Locate every blood parasite and identify its species.
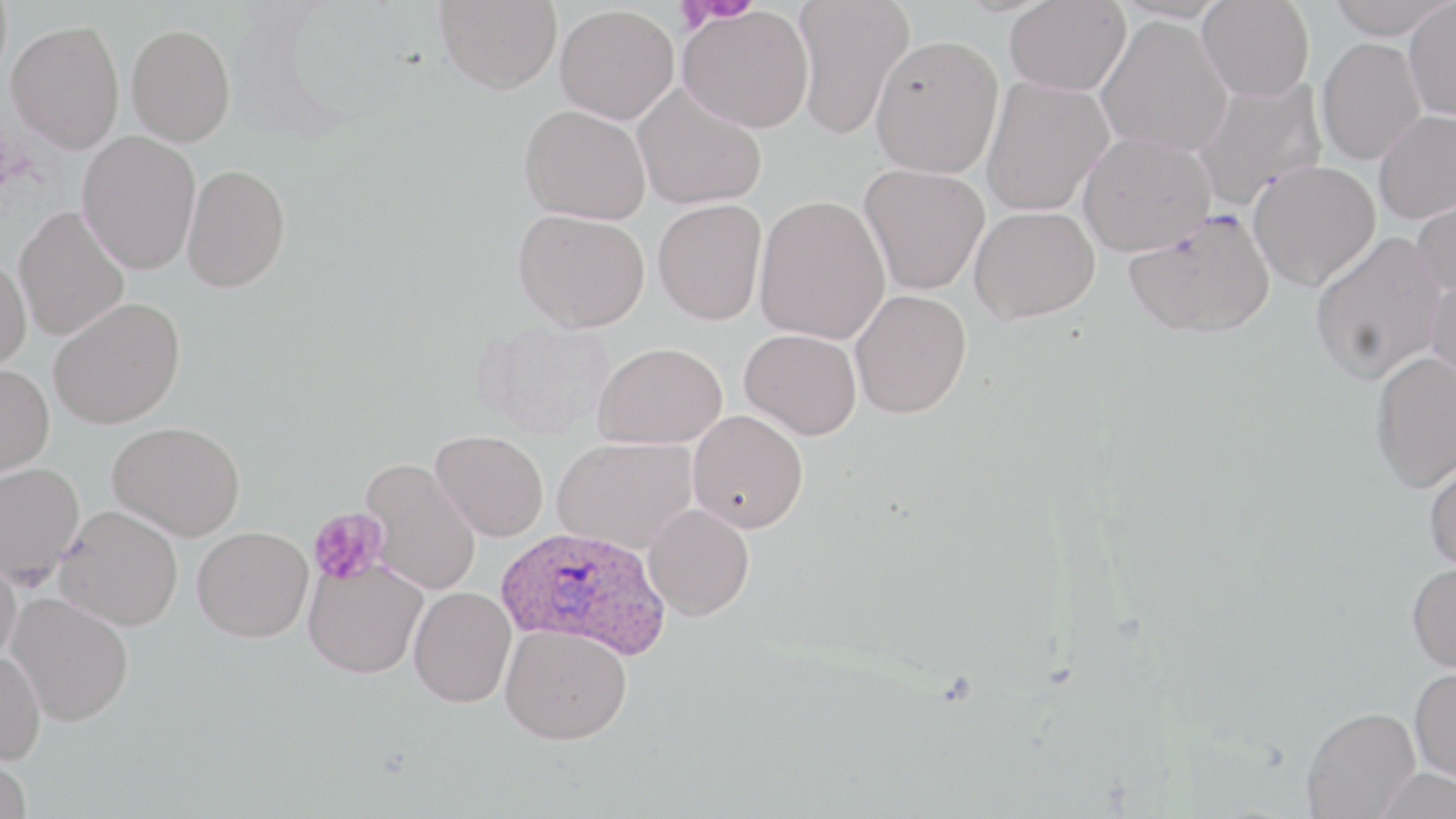

Approximate bounding boxes as named x1/y1/x2/y2 corners in pixels.
Plasmodium ovale-infected red blood cells: (x1=496, y1=526, x2=670, y2=660).
No Plasmodium falciparum, Plasmodium malariae, Plasmodium vivax, Babesia divergens, or Trypanosoma brucei observed.

slide-level diagnosis = Plasmodium ovale
field of view = one of a larger specimen
magnification = 1000x
image size = 1456×819 pixels
platelet locations = approximate bounding boxes as named x1/y1/x2/y2 corners in pixels: (x1=673, y1=0, x2=749, y2=33), (x1=308, y1=508, x2=389, y2=586)
uninfected red blood cell locations = approximate bounding boxes as named x1/y1/x2/y2 corners in pixels: (x1=435, y1=0, x2=562, y2=93), (x1=791, y1=0, x2=916, y2=140), (x1=1005, y1=0, x2=1131, y2=97), (x1=1197, y1=0, x2=1314, y2=102), (x1=1324, y1=0, x2=1455, y2=39), (x1=1403, y1=1, x2=1456, y2=120), (x1=554, y1=5, x2=678, y2=124), (x1=678, y1=6, x2=814, y2=133), (x1=1096, y1=15, x2=1233, y2=157), (x1=6, y1=20, x2=125, y2=152), (x1=126, y1=23, x2=236, y2=146), (x1=870, y1=34, x2=1003, y2=178), (x1=1316, y1=37, x2=1426, y2=165), (x1=981, y1=76, x2=1114, y2=216), (x1=1191, y1=77, x2=1327, y2=211), (x1=632, y1=82, x2=767, y2=210), (x1=519, y1=104, x2=652, y2=224), (x1=1374, y1=108, x2=1456, y2=223), (x1=77, y1=131, x2=201, y2=275), (x1=1078, y1=132, x2=1215, y2=256), (x1=1248, y1=160, x2=1381, y2=291), (x1=182, y1=163, x2=290, y2=292), (x1=859, y1=163, x2=989, y2=295), (x1=1411, y1=189, x2=1456, y2=298), (x1=755, y1=195, x2=890, y2=344), (x1=653, y1=200, x2=767, y2=325), (x1=14, y1=205, x2=129, y2=341), (x1=970, y1=206, x2=1100, y2=323), (x1=512, y1=208, x2=650, y2=333), (x1=1124, y1=208, x2=1275, y2=338), (x1=1310, y1=231, x2=1447, y2=383), (x1=0, y1=255, x2=31, y2=373), (x1=1425, y1=276, x2=1456, y2=400), (x1=850, y1=289, x2=972, y2=418), (x1=48, y1=297, x2=185, y2=430), (x1=477, y1=320, x2=615, y2=439), (x1=740, y1=328, x2=862, y2=440), (x1=594, y1=341, x2=727, y2=449), (x1=1370, y1=350, x2=1456, y2=492), (x1=0, y1=363, x2=55, y2=477), (x1=687, y1=410, x2=809, y2=533), (x1=107, y1=421, x2=246, y2=540), (x1=430, y1=429, x2=549, y2=542), (x1=553, y1=436, x2=699, y2=554), (x1=1423, y1=452, x2=1456, y2=573), (x1=361, y1=458, x2=481, y2=596), (x1=0, y1=462, x2=84, y2=587), (x1=642, y1=503, x2=754, y2=621), (x1=55, y1=505, x2=183, y2=630), (x1=191, y1=526, x2=313, y2=642), (x1=0, y1=550, x2=23, y2=666), (x1=303, y1=558, x2=428, y2=678), (x1=1407, y1=561, x2=1456, y2=673), (x1=408, y1=586, x2=516, y2=707), (x1=6, y1=592, x2=135, y2=725), (x1=501, y1=624, x2=632, y2=744), (x1=0, y1=649, x2=47, y2=765), (x1=1410, y1=665, x2=1456, y2=783), (x1=1302, y1=706, x2=1421, y2=818), (x1=0, y1=750, x2=32, y2=819), (x1=1373, y1=767, x2=1455, y2=819)
modality = optical microscopy
stain = May-Grünwald-Giemsa
preparation = thin blood smear